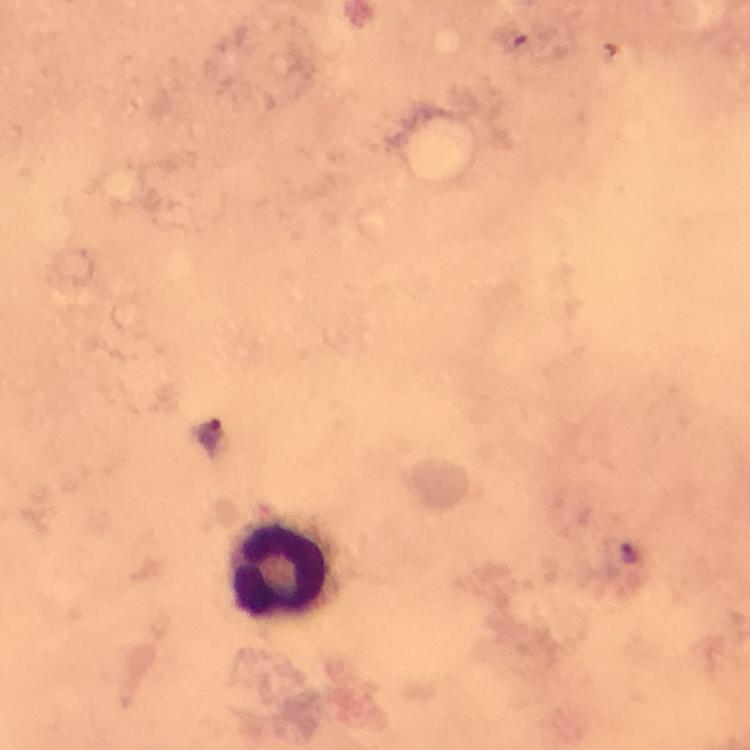 Approximate centers as {x, y} in pixels. Leukocyte locations: {281, 570}. Plasmodium parasite locations: {210, 432}. Photographed with a smartphone mounted on the microscope. At 100x magnification. Cropped region of a single field of view. Giemsa-stained preparation. Immersion oil applied. Thick blood smear. From a diagnostic examination for malaria. Image is 750×750 pixels.